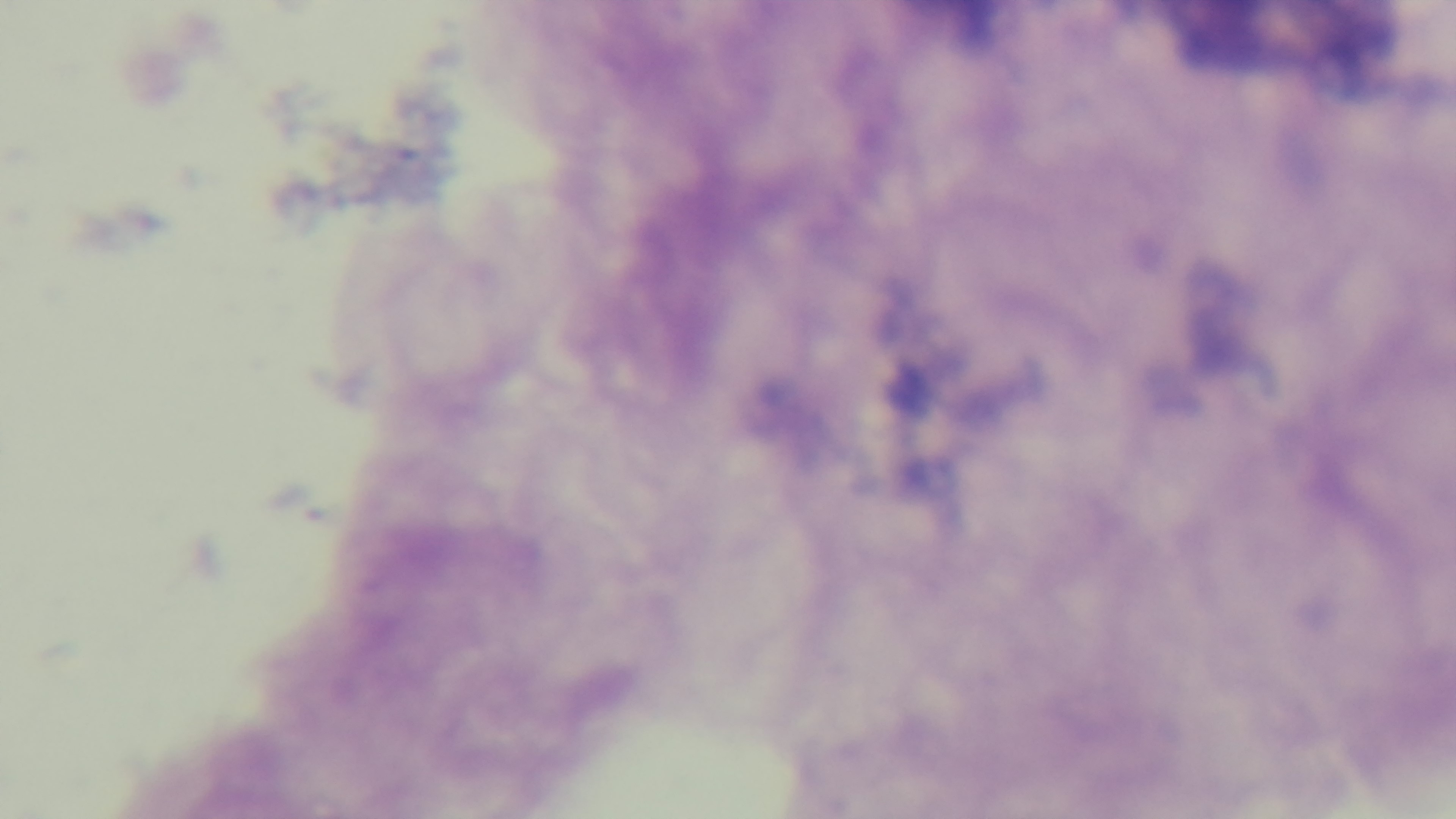
{
  "capture": "mounted 4K digital camera",
  "stain": "Giemsa",
  "modality": "light microscopy",
  "field_of_view": "one from the slide",
  "malaria_status": "uninfected",
  "preparation": "thick blood film",
  "objective": "100x oil immersion"
}